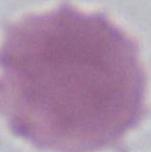 Photomicrograph. 1000x magnification. An erythrocyte is seen.